Comment on the morphology of the erythrocytes.
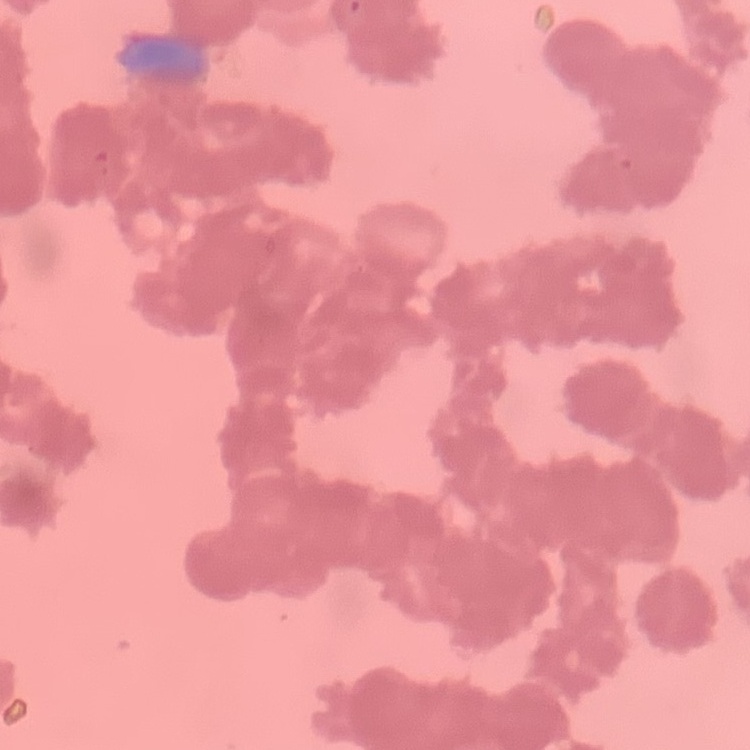
They show rouleaux formation.

One tile cut from a larger photomicrograph. Thin blood film. Stained with either Field's or Giemsa.